Classify this cell by malaria status.
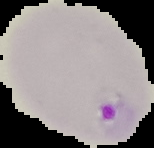

Parasitized.

Summary:
  - Image type: segmented cell region on a black background
  - Preparation: thin blood smear
  - Image size: 154×148 pixels